Point out every malaria parasite and every leukocyte.
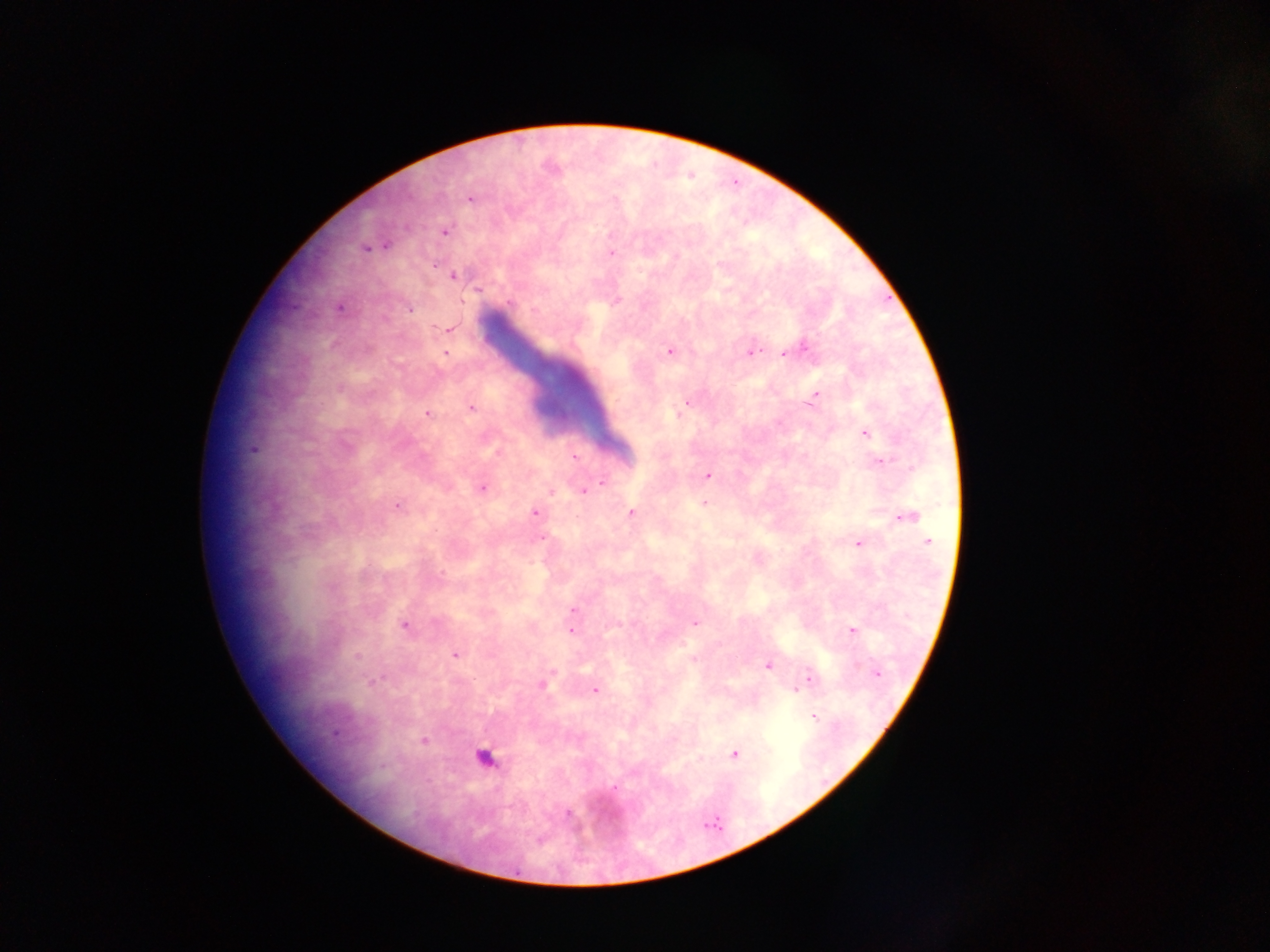

Approximate centers as [x, y] in pixels.
Malaria parasites: [469, 198], [445, 232], [386, 245], [365, 248], [611, 253], [434, 266], [453, 276], [478, 288], [617, 300], [508, 302], [339, 308], [410, 309], [535, 310], [448, 329], [804, 348], [669, 351], [750, 352], [785, 352], [446, 353], [339, 389], [815, 396], [686, 403], [471, 407], [428, 414], [865, 434], [253, 449], [575, 458], [880, 461], [709, 475], [602, 482], [594, 487], [482, 488], [584, 491], [550, 492], [705, 503], [397, 506], [631, 512], [535, 513], [907, 516], [541, 539], [927, 541], [859, 544], [573, 610], [695, 622], [404, 625], [852, 630], [571, 631], [455, 655], [357, 657], [694, 659], [768, 666], [877, 673], [810, 678], [373, 681], [543, 684], [595, 690], [796, 691], [814, 716], [335, 734], [424, 741], [734, 754], [614, 787], [568, 813].
Leukocytes: [486, 758].

Summary:
  - Preparation: thick blood smear
  - Capture: mobile-phone photograph through a microscope
  - Image size: 1270×952 pixels
  - Country: Ghana
  - Field of view: single